Report the malaria status of this cell.
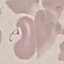

It is parasitized.

capture: smartphone camera at the microscope eyepiece
preparation: thin smear
stain: Giemsa
image_type: cell patch, automatically extracted from a larger field of view and resized to 64 × 64 pixels